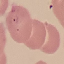
result = malaria parasites detected
stain = Giemsa
capture = smartphone through the microscope eyepiece
image type = cell patch, automatically extracted from a larger field of view and resized to 64 × 64 pixels
preparation = thin blood film